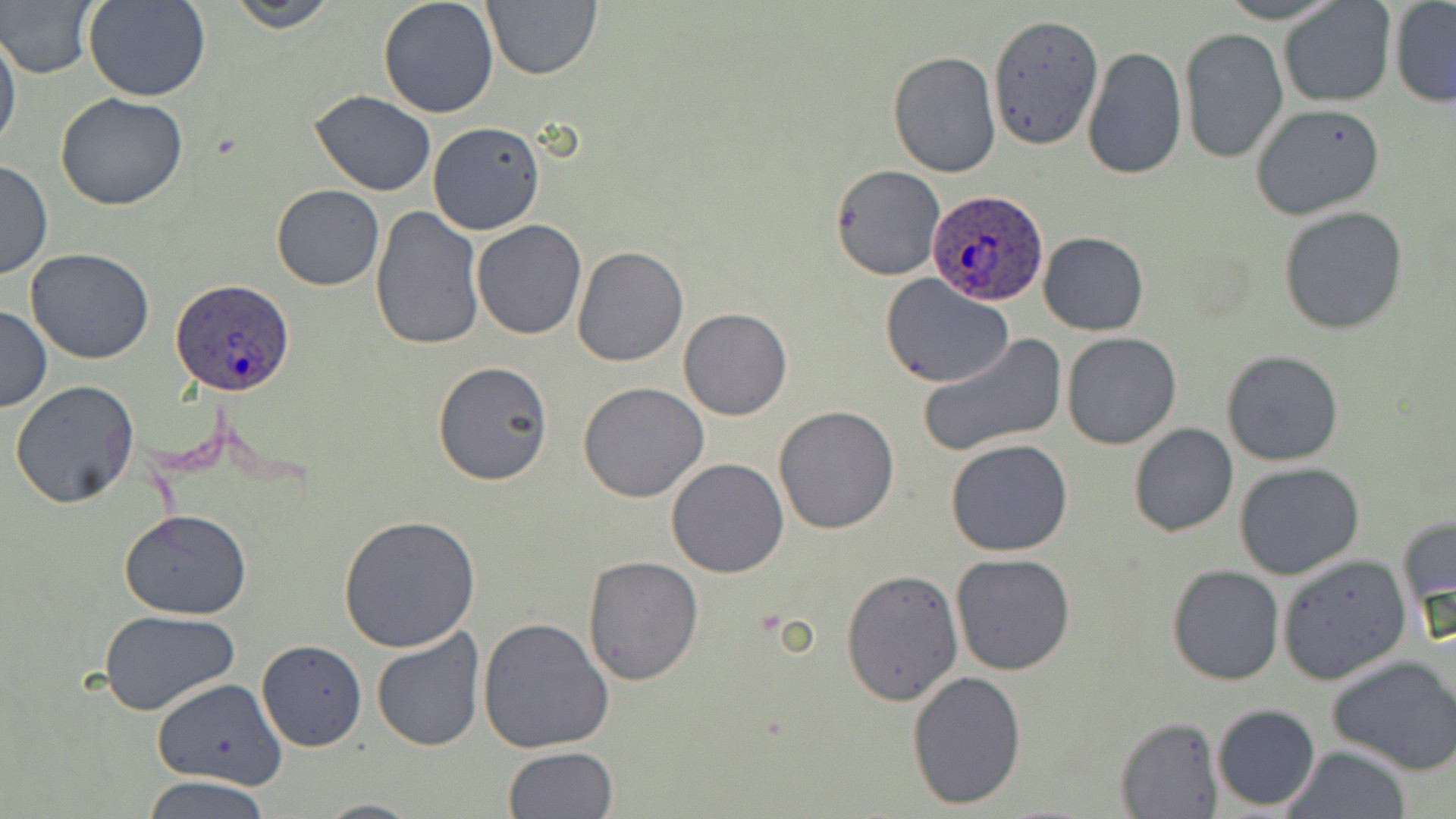

{
  "slide_level_diagnosis": "Plasmodium ovale",
  "modality": "optical microscopy",
  "magnification": "1000x",
  "preparation": "thin blood film",
  "plasmodium_ovale_infected_red_blood_cell_locations": "approximate bounding boxes as (x1,y1)-(x2,y2) corner pairs in pixels: (927,189)-(1051,305), (169,279)-(297,395)",
  "image_size": "1456×819 pixels",
  "field_of_view": "single",
  "stain": "May-Grünwald-Giemsa",
  "uninfected_red_blood_cell_locations": "approximate bounding boxes as (x1,y1)-(x2,y2) corner pairs in pixels: (2,0)-(101,80), (83,0)-(212,103), (226,0)-(341,31), (376,0)-(499,120), (481,0)-(601,81), (1215,0)-(1348,24), (1389,1)-(1456,108), (1279,2)-(1395,109), (989,13)-(1105,153), (1,28)-(22,160), (1179,28)-(1289,163), (1082,46)-(1187,179), (887,50)-(1000,178), (310,89)-(437,196), (55,91)-(188,211), (1249,102)-(1387,221), (427,121)-(545,235), (0,158)-(53,281), (829,166)-(946,281), (271,184)-(383,291), (368,206)-(488,350), (1278,206)-(1409,335), (471,219)-(587,341), (1039,232)-(1148,335), (572,246)-(688,366), (25,247)-(156,365), (878,273)-(1012,389), (0,306)-(53,412), (679,308)-(791,421), (1062,332)-(1182,449), (916,333)-(1066,460), (1221,349)-(1345,465), (431,360)-(555,487), (9,380)-(140,509), (577,381)-(709,503), (773,405)-(900,536), (1127,423)-(1238,537), (945,439)-(1074,556), (665,456)-(790,577), (1234,462)-(1365,580), (1225,467)-(1387,687), (119,508)-(253,619), (337,514)-(481,653), (1398,514)-(1456,638), (949,554)-(1076,675), (1277,554)-(1411,685), (582,555)-(705,686), (1167,565)-(1285,685), (841,568)-(965,704), (98,609)-(241,714), (477,617)-(614,753), (372,626)-(486,752), (256,640)-(368,751), (1327,654)-(1456,774), (907,670)-(1027,809), (151,677)-(286,789), (1212,704)-(1321,811), (1117,716)-(1220,818), (502,745)-(617,819), (1282,745)-(1411,819), (141,774)-(271,819), (314,797)-(424,818)"
}